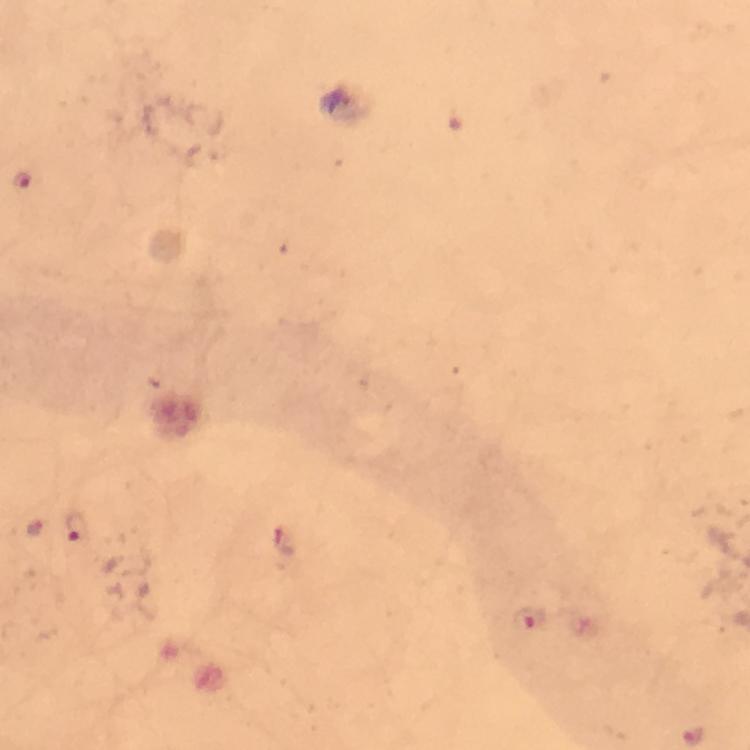
cropped from = a single field of view
capture = smartphone mounted on the microscope
stain = Giemsa
context = from a diagnostic examination for malaria
preparation = thick blood smear
malaria parasite locations = approximate object centers, in pixels from the top-left corner: (x=22, y=180), (x=33, y=526), (x=74, y=528), (x=284, y=541), (x=529, y=619), (x=693, y=736)
immersion oil = applied
image size = 750×750 pixels
magnification = 100x